Report the malaria status of this cell.
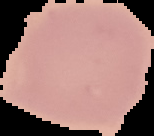
It is uninfected.

image type = segmented cell region on a black background
preparation = thin blood smear
image size = 154×136 pixels